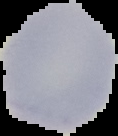

Summary:
  - Result: negative for malaria parasites
  - Image size: 118×136 pixels
  - Preparation: thin blood film
  - Image type: segmented cell region on a black background